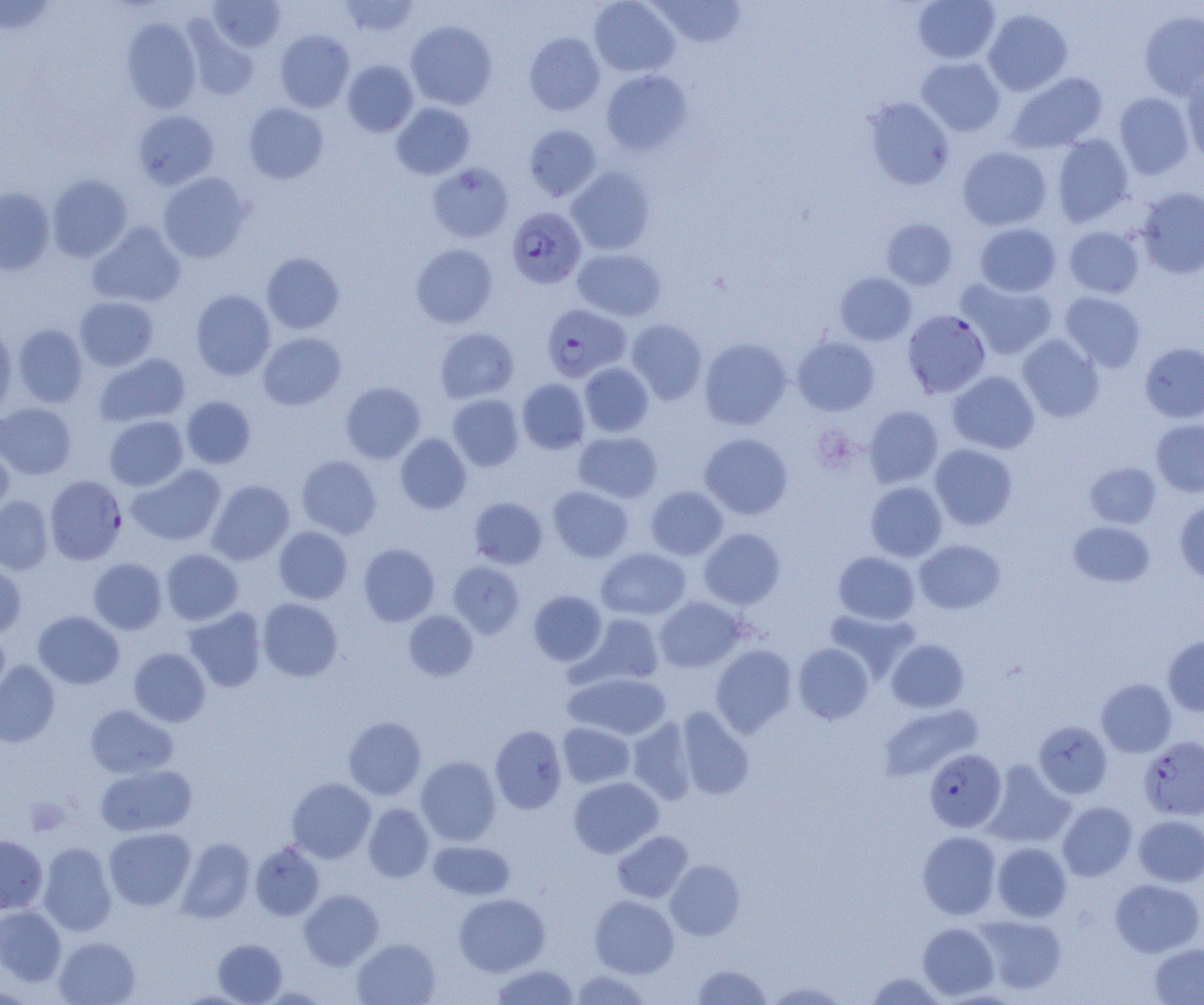
Approximate bounding boxes as (x1,y1)-(x2,y2) corner pairs in pixels. Uninfected red blood cell locations: (0,0)-(57,35), (208,0)-(285,52), (339,0)-(421,37), (589,0)-(680,77), (651,0)-(745,48), (913,0)-(1001,64), (983,9)-(1073,96), (1139,10)-(1204,99), (121,17)-(202,113), (405,21)-(497,110), (185,22)-(259,100), (274,30)-(355,112), (524,32)-(605,116), (916,57)-(1005,136), (342,60)-(418,136), (601,70)-(692,155), (1181,70)-(1204,163), (1006,72)-(1108,153), (1114,92)-(1194,179), (864,97)-(954,190), (391,102)-(475,179), (243,103)-(329,184), (134,110)-(218,189), (524,124)-(602,201), (1052,134)-(1134,226), (957,146)-(1052,230), (427,162)-(514,243), (566,166)-(656,255), (158,172)-(251,262), (47,174)-(132,262), (0,187)-(55,275), (1136,187)-(1204,278), (881,218)-(958,290), (87,222)-(186,308), (974,223)-(1061,296), (1063,225)-(1144,299), (411,243)-(498,328), (572,248)-(666,321), (261,253)-(344,334), (835,272)-(917,345), (957,278)-(1057,360), (191,290)-(275,380), (1060,291)-(1146,372), (74,296)-(158,370), (627,319)-(707,404), (0,321)-(16,415), (13,324)-(88,407), (435,328)-(519,403), (258,332)-(346,410), (1017,334)-(1104,422), (792,336)-(879,416), (699,337)-(791,430), (1140,342)-(1204,422), (94,353)-(190,427), (579,362)-(653,437), (946,371)-(1040,454), (517,378)-(590,454), (341,382)-(426,463), (448,394)-(524,471), (181,396)-(256,469), (0,403)-(76,479), (864,405)-(944,488), (104,415)-(188,490), (1151,419)-(1204,497), (573,431)-(663,503), (395,433)-(471,513), (699,433)-(793,519), (0,442)-(14,519), (930,443)-(1018,530), (296,455)-(381,538), (1084,461)-(1161,529), (127,464)-(226,546), (206,480)-(294,565), (865,481)-(947,562), (547,485)-(633,562), (646,485)-(727,559), (0,495)-(53,575), (469,497)-(548,569), (1175,501)-(1204,584), (1068,520)-(1155,587), (274,526)-(352,604), (699,528)-(785,609), (913,539)-(1006,614), (358,543)-(440,626), (160,548)-(243,625), (596,548)-(691,620), (833,551)-(920,625), (88,558)-(167,634), (448,561)-(524,638), (0,562)-(26,639), (529,591)-(607,666), (654,596)-(746,672), (257,598)-(343,682), (183,607)-(267,692), (824,608)-(919,681), (403,610)-(478,681), (33,611)-(124,689), (580,613)-(665,687), (0,632)-(10,710), (1163,635)-(1204,716), (887,639)-(969,713), (793,643)-(874,724), (711,644)-(797,737), (128,648)-(210,726), (0,660)-(60,747), (564,672)-(671,739), (1096,678)-(1177,757), (878,703)-(982,781), (85,704)-(178,778), (676,707)-(754,800), (343,716)-(426,799), (627,717)-(697,804), (1033,721)-(1113,799), (558,722)-(635,788), (490,725)-(568,814), (415,756)-(501,845), (983,761)-(1075,848), (95,764)-(197,837), (568,776)-(663,858), (287,778)-(376,863), (1057,802)-(1137,881), (363,804)-(434,882), (1133,815)-(1204,887), (104,827)-(195,911), (612,830)-(694,903), (917,831)-(1001,919), (0,835)-(48,914), (176,837)-(255,923), (428,840)-(515,900), (250,841)-(325,921), (992,842)-(1071,922), (38,843)-(116,936), (665,859)-(745,940), (1110,879)-(1204,957), (299,889)-(383,970), (454,892)-(550,976), (589,895)-(679,978), (0,905)-(66,987), (974,914)-(1067,995), (918,922)-(998,1000), (54,936)-(140,1005), (352,938)-(440,1005), (213,939)-(287,1004), (1148,943)-(1204,1004), (692,963)-(773,1004), (491,964)-(579,1004), (571,970)-(651,1005), (866,972)-(946,1005), (765,980)-(852,1004). Platelet locations: (25,798)-(69,836). Plasmodium falciparum-infected red blood cell locations: (507,206)-(586,288), (541,304)-(631,382), (903,309)-(991,398), (45,476)-(126,565), (1139,736)-(1204,820), (925,749)-(1006,832). Slide-level diagnosis: Plasmodium falciparum. Single field of view. Image is 1204×1005 pixels. Optical microscopy. Thin blood film. 1000x magnification.